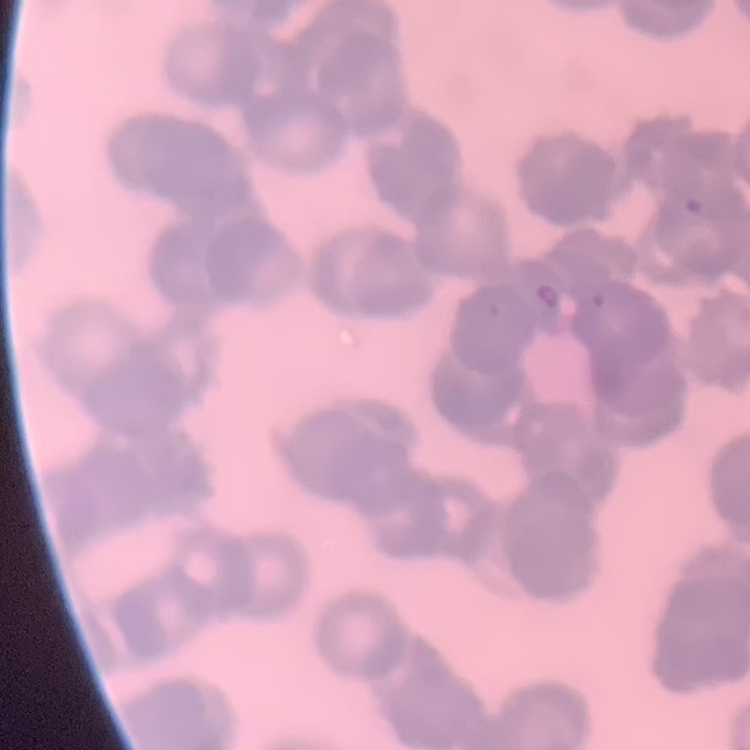
red blood cell morphology = rouleaux formation
image type = one tile cut from a larger photomicrograph
preparation = thin peripheral smear
stain = Field's or Giemsa